Assess this cell for malaria.
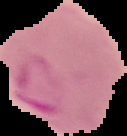
It is parasitized.

preparation = thin blood smear
image type = segmented cell region with the area outside set to black
image size = 127×136 pixels